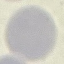

malaria status = uninfected
capture = smartphone through the microscope eyepiece
preparation = thin blood film
stain = Giemsa
image type = automatically extracted cell patch, resized to 64 × 64 pixels